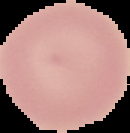
{
  "image_type": "cell region segmented out of the field of view; surrounding area masked to black",
  "image_size": "130×133 pixels",
  "preparation": "thin blood smear",
  "malaria_status": "uninfected"
}